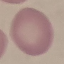

result = no malaria parasites seen
capture = smartphone through the microscope eyepiece
stain = Giemsa
preparation = thin blood smear
image type = automatically extracted cell patch, resized to 64 × 64 pixels